Comment on the morphology of the erythrocytes.
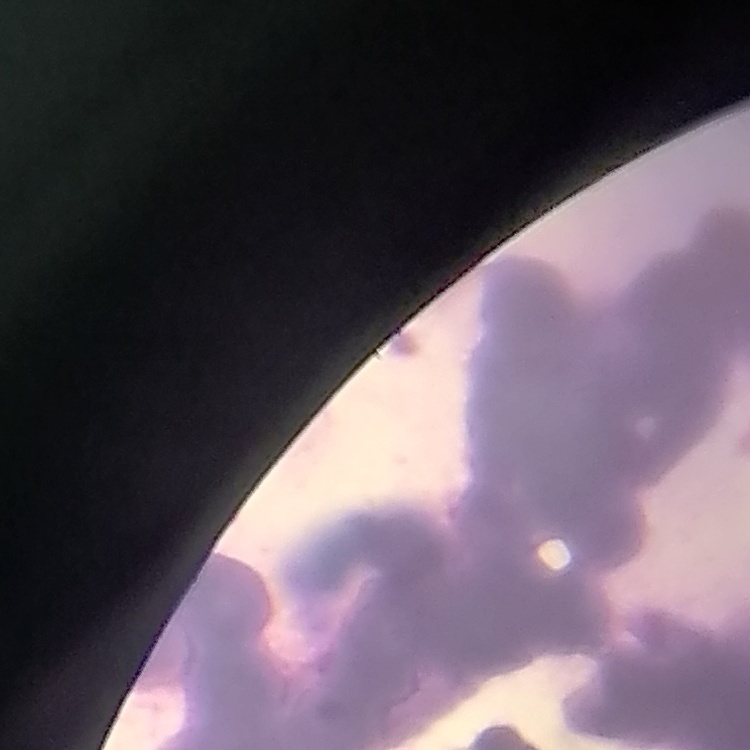

Rouleaux formation.

One tile cut from a larger photomicrograph. Thin blood film. Field's or Giemsa stain.